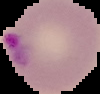

{
  "image_type": "cell region segmented out of the field of view; surrounding area masked to black",
  "image_size": "100×94 pixels",
  "preparation": "thin blood smear",
  "malaria_status": "parasitized"
}